Report the malaria status of this cell.
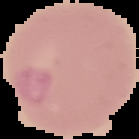

Uninfected.

Summary:
  - Image type: cell region segmented out of the field of view; surrounding area masked to black
  - Preparation: thin blood smear
  - Image size: 139×139 pixels